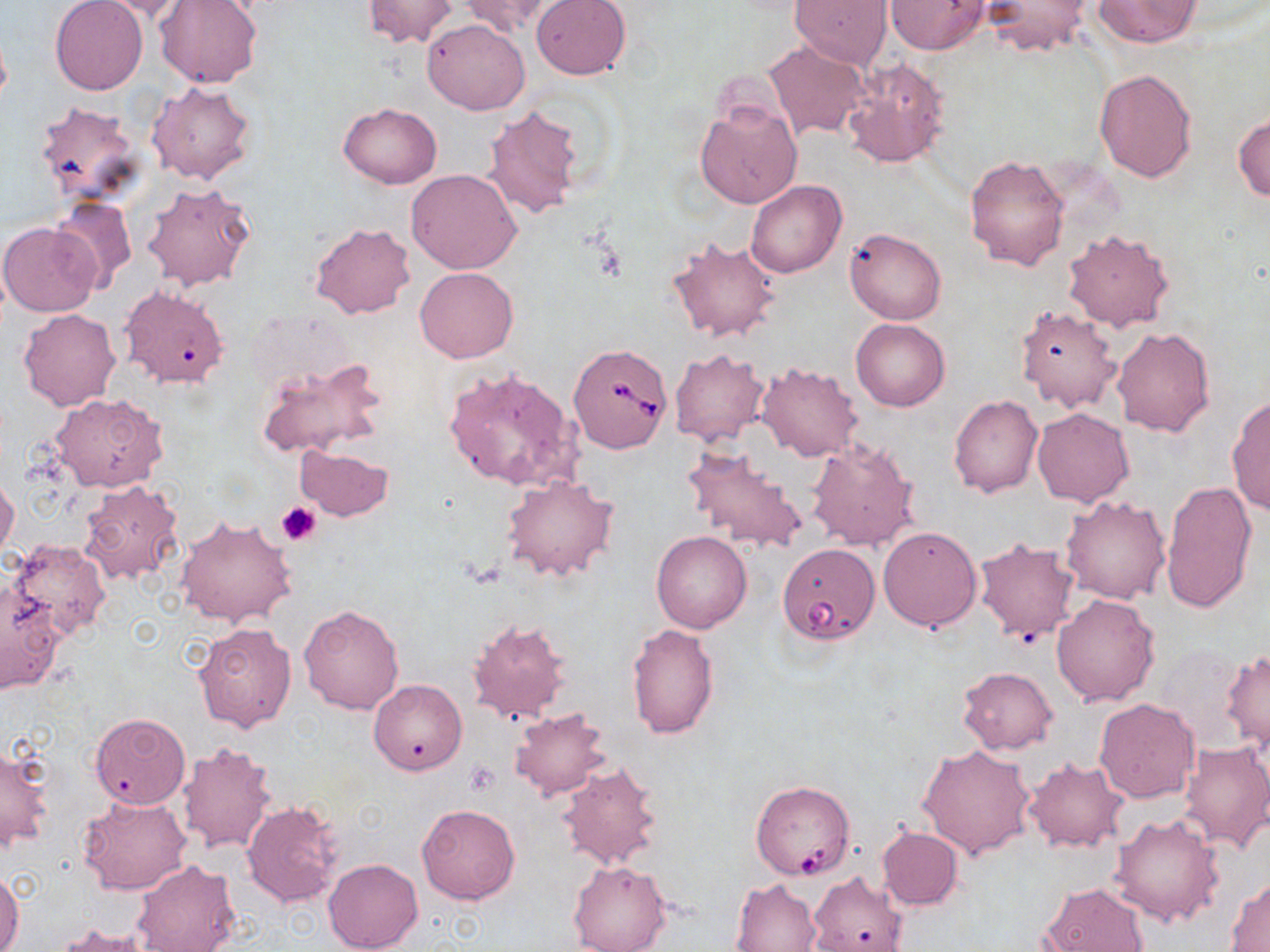

Approximate bounding boxes as named x1/y1/x2/y2 corners in pixels. Platelet locations: (x1=276, y1=501, x2=322, y2=545), (x1=463, y1=763, x2=500, y2=795). Uninfected red blood cell locations: (x1=49, y1=0, x2=148, y2=96), (x1=89, y1=0, x2=193, y2=21), (x1=363, y1=0, x2=457, y2=48), (x1=461, y1=0, x2=559, y2=37), (x1=531, y1=0, x2=631, y2=80), (x1=792, y1=0, x2=892, y2=67), (x1=885, y1=0, x2=990, y2=54), (x1=156, y1=1, x2=262, y2=89), (x1=979, y1=1, x2=1095, y2=57), (x1=1092, y1=1, x2=1204, y2=48), (x1=423, y1=18, x2=528, y2=115), (x1=762, y1=39, x2=872, y2=142), (x1=843, y1=57, x2=951, y2=168), (x1=1095, y1=67, x2=1197, y2=182), (x1=147, y1=81, x2=257, y2=184), (x1=695, y1=99, x2=802, y2=209), (x1=33, y1=100, x2=144, y2=207), (x1=339, y1=103, x2=442, y2=187), (x1=482, y1=104, x2=584, y2=220), (x1=1232, y1=114, x2=1270, y2=202), (x1=966, y1=154, x2=1070, y2=272), (x1=406, y1=168, x2=521, y2=274), (x1=747, y1=179, x2=846, y2=278), (x1=142, y1=182, x2=256, y2=290), (x1=48, y1=195, x2=137, y2=290), (x1=0, y1=221, x2=102, y2=316), (x1=311, y1=222, x2=416, y2=319), (x1=845, y1=226, x2=947, y2=324), (x1=1063, y1=229, x2=1175, y2=332), (x1=667, y1=235, x2=780, y2=344), (x1=416, y1=267, x2=518, y2=363), (x1=119, y1=286, x2=231, y2=389), (x1=1015, y1=305, x2=1121, y2=412), (x1=18, y1=309, x2=121, y2=411), (x1=851, y1=318, x2=950, y2=412), (x1=1112, y1=326, x2=1214, y2=436), (x1=670, y1=348, x2=771, y2=447), (x1=256, y1=357, x2=386, y2=460), (x1=755, y1=362, x2=863, y2=461), (x1=446, y1=368, x2=581, y2=519), (x1=50, y1=392, x2=167, y2=491), (x1=1227, y1=394, x2=1270, y2=513), (x1=948, y1=395, x2=1043, y2=498), (x1=1033, y1=407, x2=1133, y2=506), (x1=806, y1=438, x2=920, y2=551), (x1=682, y1=443, x2=809, y2=553), (x1=294, y1=446, x2=395, y2=522), (x1=0, y1=475, x2=20, y2=562), (x1=501, y1=475, x2=620, y2=582), (x1=79, y1=478, x2=184, y2=588), (x1=1162, y1=479, x2=1258, y2=615), (x1=1061, y1=495, x2=1172, y2=604), (x1=175, y1=515, x2=297, y2=628), (x1=877, y1=525, x2=982, y2=631), (x1=652, y1=532, x2=751, y2=633), (x1=973, y1=537, x2=1079, y2=642), (x1=8, y1=539, x2=112, y2=638), (x1=0, y1=585, x2=65, y2=694), (x1=1051, y1=593, x2=1160, y2=706), (x1=299, y1=603, x2=405, y2=716), (x1=467, y1=618, x2=573, y2=724), (x1=193, y1=623, x2=296, y2=732), (x1=626, y1=623, x2=719, y2=739), (x1=1224, y1=651, x2=1270, y2=752), (x1=958, y1=666, x2=1059, y2=754), (x1=369, y1=678, x2=468, y2=775), (x1=1095, y1=698, x2=1198, y2=803), (x1=509, y1=707, x2=613, y2=800), (x1=89, y1=713, x2=190, y2=808), (x1=1179, y1=741, x2=1270, y2=852), (x1=179, y1=742, x2=279, y2=856), (x1=916, y1=743, x2=1036, y2=859), (x1=0, y1=746, x2=54, y2=851), (x1=1023, y1=758, x2=1127, y2=852), (x1=555, y1=760, x2=666, y2=871), (x1=78, y1=795, x2=192, y2=897), (x1=241, y1=798, x2=347, y2=908), (x1=417, y1=804, x2=520, y2=904), (x1=1109, y1=812, x2=1225, y2=927), (x1=877, y1=827, x2=963, y2=910), (x1=323, y1=857, x2=423, y2=952), (x1=130, y1=859, x2=241, y2=952), (x1=567, y1=859, x2=671, y2=952), (x1=0, y1=869, x2=24, y2=952), (x1=806, y1=871, x2=909, y2=952), (x1=1227, y1=877, x2=1270, y2=950), (x1=730, y1=878, x2=821, y2=951), (x1=1040, y1=881, x2=1149, y2=952), (x1=55, y1=922, x2=155, y2=951). Babesia divergens-infected red blood cell locations: (x1=570, y1=343, x2=672, y2=454), (x1=778, y1=543, x2=879, y2=644), (x1=751, y1=779, x2=855, y2=880). Slide-level diagnosis: Babesia divergens. Thin blood smear. Optical microscopy. One field of a larger specimen. Image is 1270×952 pixels. 1000x magnification. May-Grünwald-Giemsa stain.